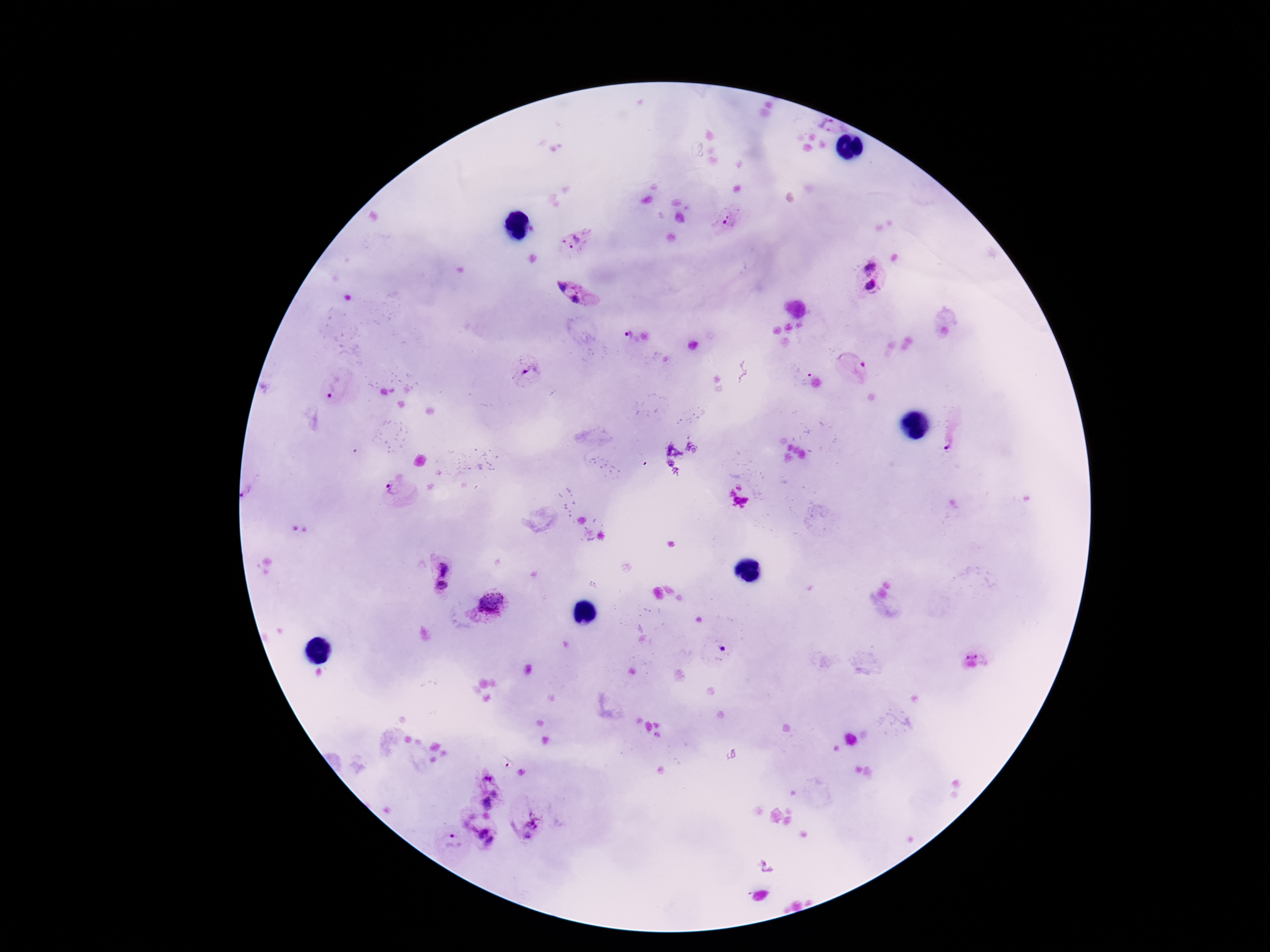
Approximate object centers, in pixels from the top-left corner.
Summary:
  - Plasmodium parasite locations: (x=830, y=126), (x=727, y=220), (x=575, y=241), (x=871, y=267), (x=872, y=286), (x=562, y=287), (x=581, y=299), (x=626, y=335), (x=856, y=369), (x=526, y=371), (x=799, y=374), (x=334, y=388), (x=952, y=440), (x=396, y=488), (x=443, y=567), (x=442, y=588), (x=490, y=605), (x=721, y=650), (x=977, y=652), (x=487, y=793), (x=529, y=819), (x=483, y=829), (x=451, y=840), (x=766, y=867)
  - Magnification: 100x
  - Capture: smartphone camera through the microscope eyepiece
  - Field of view: one from this slide
  - Stain: Giemsa
  - Preparation: thick peripheral-blood smear
  - Image size: 1270×952 pixels
  - Patient malaria status: infected